Identify the blood parasite species.
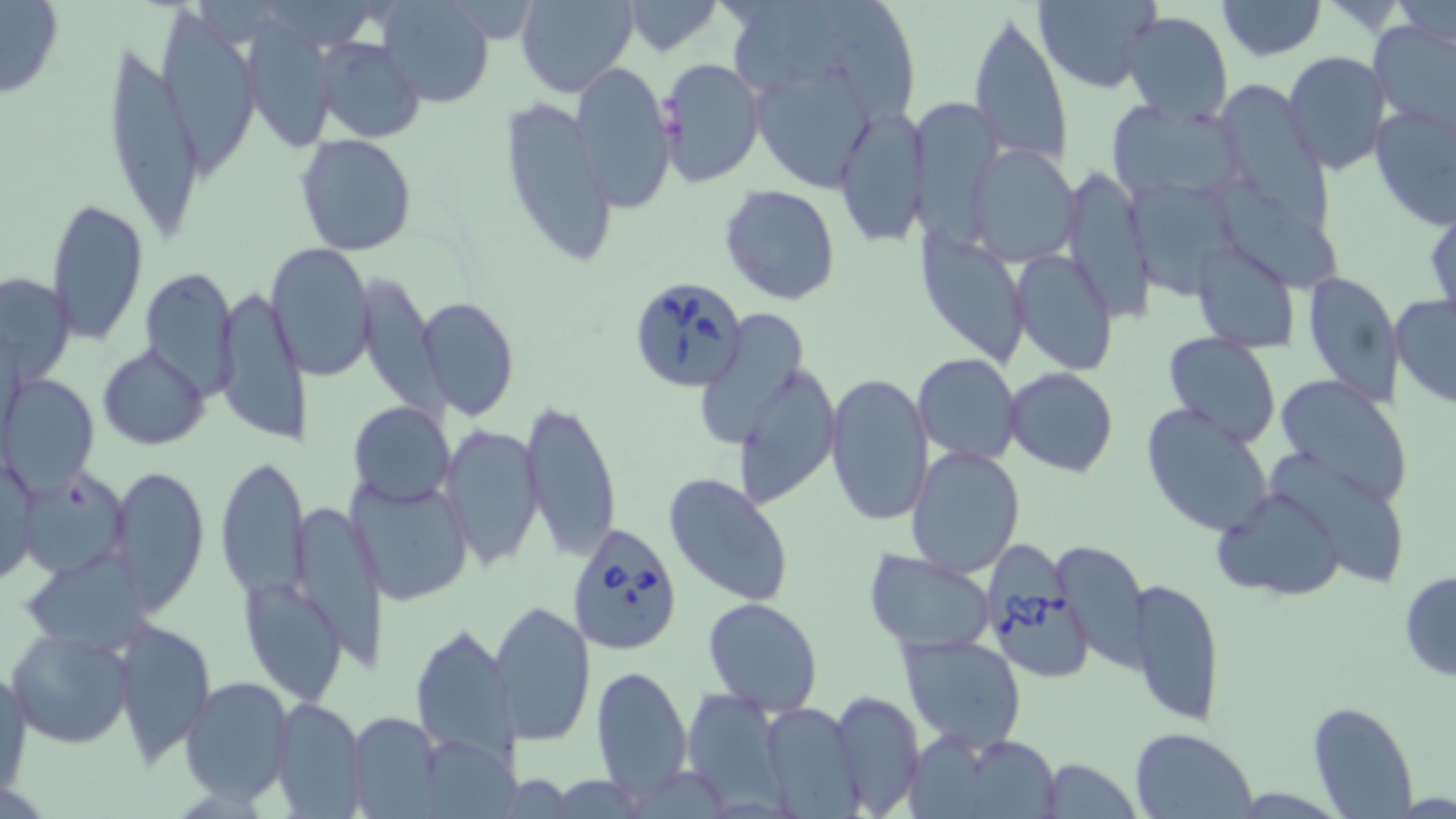

Babesia divergens.

image size = 1456×819 pixels
stain = May-Grünwald-Giemsa
field of view = single
magnification = 1000x
uninfected red blood cell locations = approximate bounding boxes as [x1, y1, x2, y2] in pixels: [377, 0, 494, 108], [516, 0, 638, 99], [619, 0, 724, 56], [823, 0, 915, 130], [1034, 0, 1164, 94], [1216, 0, 1325, 59], [0, 2, 64, 97], [734, 2, 859, 93], [1390, 2, 1456, 52], [158, 9, 260, 181], [966, 11, 1073, 167], [1119, 11, 1232, 124], [242, 15, 333, 147], [1372, 20, 1456, 130], [315, 36, 426, 143], [100, 40, 215, 240], [1283, 51, 1390, 174], [659, 57, 765, 187], [571, 62, 676, 212], [749, 70, 874, 194], [1220, 84, 1334, 238], [499, 92, 618, 268], [1106, 100, 1250, 209], [1370, 101, 1456, 229], [915, 102, 1001, 254], [833, 106, 926, 248], [295, 135, 417, 255], [966, 142, 1080, 266], [1057, 163, 1152, 323], [1121, 180, 1239, 296], [1218, 180, 1346, 296], [720, 184, 842, 306], [46, 201, 148, 344], [917, 228, 1025, 373], [1194, 238, 1300, 352], [265, 243, 376, 381], [1011, 250, 1116, 376], [137, 267, 240, 395], [1303, 271, 1403, 407], [2, 272, 74, 386], [358, 280, 456, 430], [214, 284, 309, 446], [1389, 292, 1456, 409], [414, 297, 521, 421], [694, 309, 811, 451], [1162, 333, 1282, 447], [97, 345, 211, 449], [913, 354, 1021, 464], [736, 361, 840, 505], [1005, 367, 1118, 476], [824, 370, 934, 528], [2, 374, 98, 494], [1273, 374, 1414, 507], [520, 397, 621, 561], [349, 401, 455, 509], [1140, 402, 1276, 537], [440, 425, 544, 568], [906, 445, 1028, 579], [214, 456, 311, 605], [0, 460, 42, 589], [111, 465, 207, 612], [15, 470, 129, 575], [662, 472, 795, 607], [352, 475, 476, 605], [1213, 486, 1348, 600], [287, 499, 388, 673], [1053, 539, 1149, 668], [864, 549, 996, 654], [25, 557, 151, 654], [1399, 571, 1456, 681], [1128, 579, 1226, 728], [243, 580, 349, 706], [703, 597, 822, 716], [489, 601, 597, 746], [110, 617, 216, 766], [410, 622, 518, 759], [6, 625, 133, 748], [899, 633, 1027, 749], [591, 663, 692, 801], [1, 665, 31, 796], [180, 674, 295, 805], [682, 688, 787, 810], [830, 688, 925, 817], [269, 697, 366, 818], [1307, 700, 1419, 818], [759, 702, 860, 817], [344, 710, 446, 817], [1130, 727, 1258, 819], [940, 733, 1064, 819], [1037, 757, 1143, 819]
Babesia divergens-infected red blood cell locations = approximate bounding boxes as [x1, y1, x2, y2] in pixels: [628, 274, 747, 392], [567, 522, 685, 656], [987, 543, 1093, 682]
preparation = thin blood smear
modality = optical microscopy